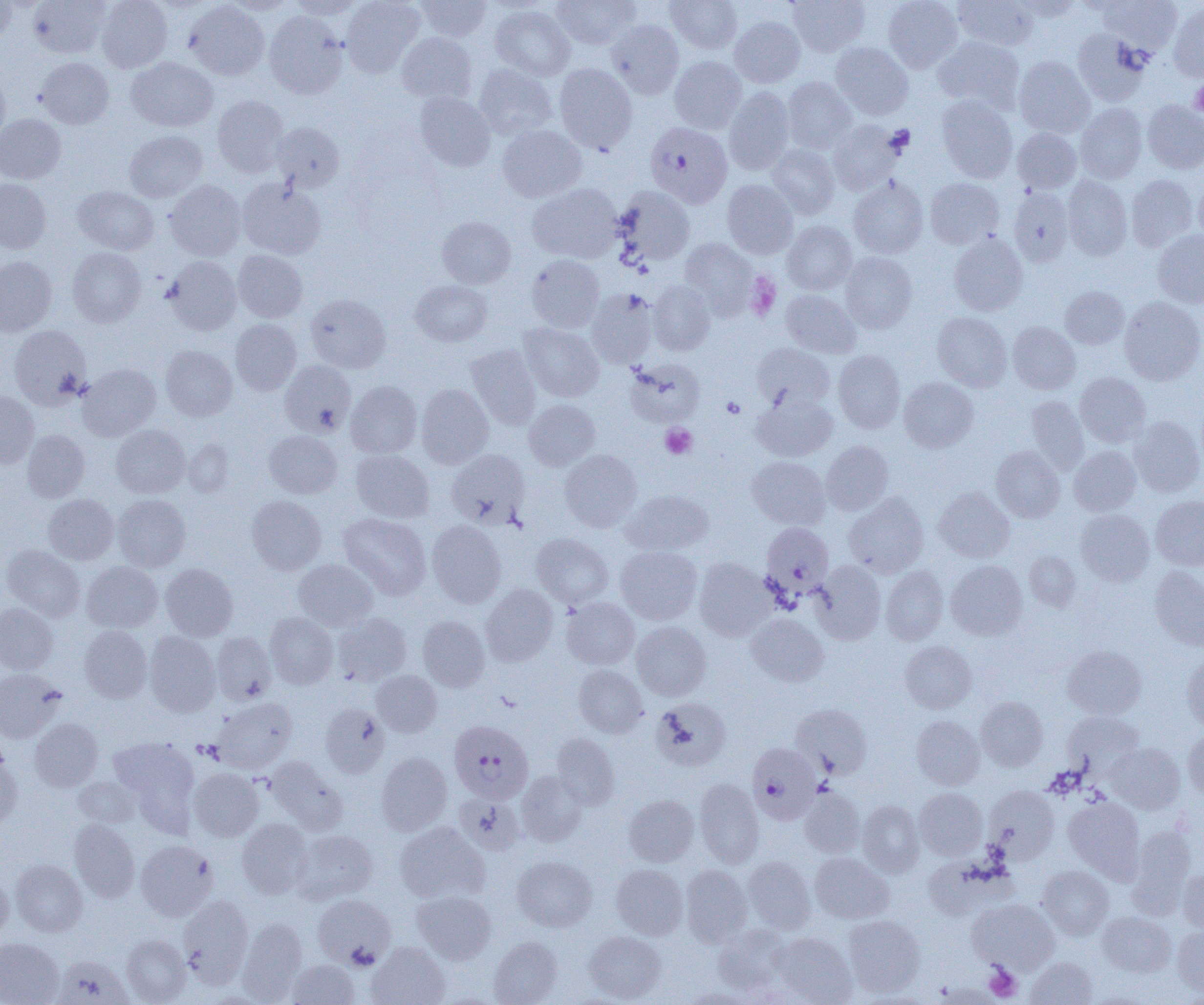

slide-level diagnosis = Plasmodium falciparum
field of view = one of a larger specimen
uninfected red blood cell locations = approximate bounding boxes as [x1, y1, x2, y2] in pixels: [28, 0, 111, 58], [96, 0, 172, 73], [289, 0, 364, 20], [341, 0, 424, 77], [416, 0, 492, 42], [666, 0, 742, 53], [787, 0, 869, 57], [882, 0, 963, 72], [954, 0, 1039, 50], [1098, 0, 1182, 53], [0, 1, 17, 44], [184, 1, 269, 81], [552, 1, 640, 50], [1168, 3, 1204, 82], [490, 4, 575, 81], [264, 11, 348, 99], [730, 16, 805, 87], [606, 19, 685, 99], [1073, 29, 1151, 106], [396, 32, 477, 104], [933, 36, 1025, 112], [831, 43, 913, 120], [669, 56, 747, 133], [1014, 56, 1094, 138], [36, 57, 114, 129], [126, 57, 218, 132], [554, 63, 637, 153], [473, 64, 558, 140], [0, 76, 9, 147], [782, 76, 857, 154], [724, 87, 794, 174], [414, 92, 495, 171], [213, 95, 288, 177], [936, 95, 1018, 183], [1143, 100, 1204, 174], [1075, 103, 1148, 183], [0, 113, 66, 184], [828, 120, 903, 195], [273, 122, 344, 190], [497, 125, 587, 203], [1012, 128, 1081, 193], [124, 130, 208, 203], [767, 144, 839, 218], [1062, 175, 1132, 260], [1126, 175, 1199, 251], [849, 177, 928, 258], [925, 177, 1004, 249], [1194, 177, 1204, 247], [237, 178, 326, 260], [0, 179, 51, 253], [165, 179, 246, 261], [722, 180, 799, 259], [527, 183, 622, 263], [614, 186, 695, 267], [72, 187, 159, 255], [1009, 188, 1074, 266], [437, 216, 516, 289], [782, 221, 857, 295], [1152, 230, 1204, 308], [948, 234, 1027, 316], [680, 238, 757, 318], [67, 247, 146, 327], [233, 250, 308, 322], [840, 252, 917, 333], [527, 254, 605, 332], [0, 256, 56, 336], [163, 256, 242, 336], [410, 280, 493, 346], [648, 280, 716, 356], [1061, 286, 1129, 349], [586, 288, 658, 368], [780, 290, 861, 358], [306, 294, 391, 373], [1119, 296, 1204, 385], [932, 312, 1012, 392], [231, 319, 302, 395], [1008, 321, 1080, 394], [519, 322, 604, 402], [9, 325, 91, 409], [752, 343, 834, 410], [160, 345, 237, 421], [465, 345, 542, 429], [833, 350, 906, 433], [625, 358, 706, 427], [279, 360, 356, 436], [78, 364, 161, 441], [1075, 371, 1150, 447], [899, 377, 978, 452], [346, 380, 422, 458], [416, 384, 494, 468], [0, 391, 39, 468], [752, 393, 837, 461], [1026, 395, 1089, 473], [524, 399, 600, 470], [1129, 416, 1204, 497], [111, 424, 189, 498], [22, 429, 90, 502], [264, 430, 342, 498], [183, 440, 233, 496], [820, 440, 893, 515], [1069, 445, 1141, 515], [991, 446, 1065, 522], [351, 449, 434, 522], [446, 449, 530, 529], [560, 449, 642, 532], [747, 456, 830, 530], [934, 487, 1015, 562], [621, 489, 713, 556], [844, 493, 929, 578], [43, 494, 119, 565], [113, 494, 190, 571], [1150, 495, 1204, 570], [246, 496, 326, 575], [1075, 509, 1154, 586], [338, 513, 431, 600], [427, 520, 506, 608], [531, 533, 613, 608], [2, 545, 85, 621], [615, 546, 702, 625], [1024, 551, 1081, 612], [695, 558, 774, 641], [293, 559, 377, 631], [811, 560, 886, 644], [946, 560, 1028, 640], [81, 561, 163, 632], [160, 563, 238, 641], [881, 565, 949, 645], [1150, 565, 1204, 650], [481, 584, 558, 666], [561, 596, 639, 669], [0, 603, 58, 673], [265, 612, 338, 688], [333, 612, 412, 686], [746, 613, 828, 687], [418, 615, 489, 691], [631, 621, 711, 700], [79, 625, 152, 703], [144, 631, 221, 717], [211, 632, 276, 705], [900, 641, 977, 714], [1062, 645, 1147, 719], [1182, 652, 1204, 730], [573, 664, 648, 738], [0, 668, 66, 743], [371, 670, 442, 737], [976, 696, 1048, 770], [212, 697, 297, 774], [652, 698, 731, 770], [320, 703, 389, 778], [790, 704, 872, 778], [1063, 711, 1144, 775], [911, 715, 984, 790], [30, 718, 103, 791], [1183, 729, 1204, 801], [551, 733, 620, 809], [109, 736, 199, 816], [1106, 743, 1185, 813], [0, 748, 21, 832], [377, 752, 451, 835], [265, 756, 348, 835], [188, 767, 263, 841], [516, 770, 588, 846], [74, 776, 141, 827], [694, 778, 764, 868], [983, 785, 1060, 863], [799, 786, 864, 857], [914, 787, 988, 860], [454, 793, 524, 855], [624, 795, 699, 866], [1063, 797, 1144, 880], [857, 801, 924, 877], [236, 818, 313, 899], [69, 819, 140, 902], [394, 821, 489, 904], [1127, 825, 1195, 915], [292, 829, 377, 904], [135, 840, 218, 921], [810, 852, 894, 924], [512, 855, 597, 931], [742, 856, 816, 934], [10, 859, 87, 936], [611, 864, 688, 939], [680, 865, 753, 947], [1037, 866, 1113, 939], [1179, 869, 1204, 934], [0, 870, 13, 943], [412, 891, 496, 963], [312, 893, 395, 968], [177, 894, 253, 986], [968, 898, 1059, 973], [1097, 911, 1175, 977], [843, 915, 925, 997], [237, 918, 308, 1003], [713, 924, 792, 996], [1173, 925, 1204, 997], [583, 930, 666, 1002], [772, 932, 856, 1004], [121, 934, 191, 1004], [488, 936, 562, 1005], [0, 937, 64, 1005], [367, 942, 450, 1005], [53, 955, 133, 1005], [1026, 957, 1097, 1005], [286, 959, 360, 1004], [682, 988, 761, 1004]
preparation = thin blood smear
magnification = 1000x
Plasmodium falciparum-infected red blood cell locations = approximate bounding boxes as [x1, y1, x2, y2] in pixels: [647, 124, 730, 211], [760, 522, 834, 597], [449, 720, 533, 803], [747, 742, 821, 824]
modality = optical microscopy
platelet locations = approximate bounding boxes as [x1, y1, x2, y2] in pixels: [1190, 79, 1204, 117], [744, 272, 780, 321], [722, 397, 745, 418], [660, 424, 697, 459], [984, 963, 1022, 1001]
image size = 1204×1005 pixels